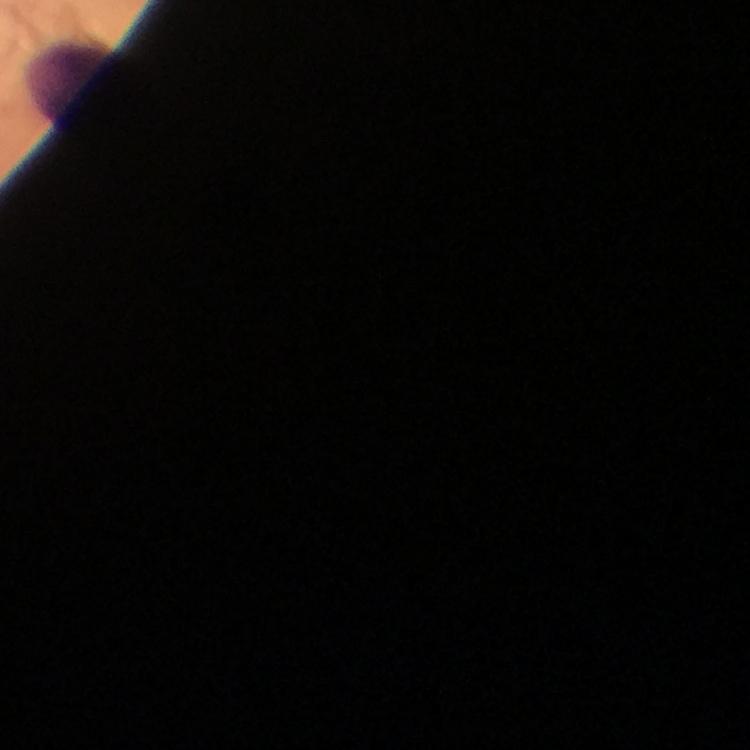
Approximate centers as {x, y} in pixels.
Summary:
  - Leukocyte locations: {72, 81}
  - Preparation: thick blood smear
  - Stain: Giemsa
  - Magnification: 100x
  - Plasmodium parasites: none detected
  - Image size: 750×750 pixels
  - Context: from a malaria diagnostic workup
  - Cropped from: one field of view
  - Capture: smartphone camera through the microscope
  - Immersion oil: applied